Identify the parasite.
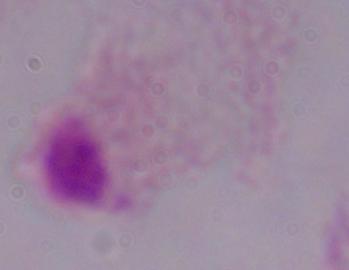
A trichomonad.

1000x magnification. Micrograph.